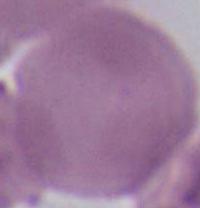
modality: photomicrograph
magnification: 1000x
identification: red blood cell